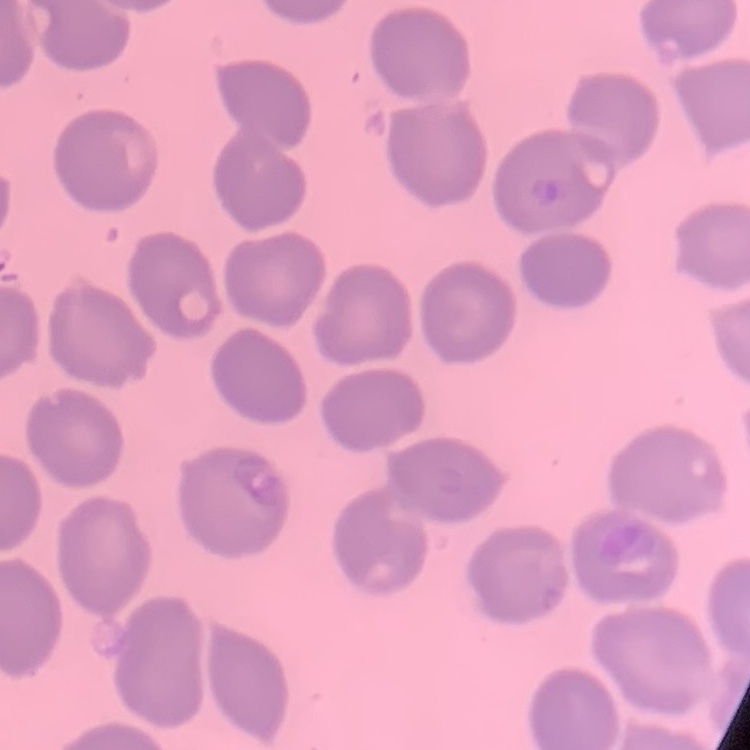
The red blood cells show no rouleaux formation. Stained with either Field's or Giemsa. Thin blood film. Square crop of a larger photomicrograph.